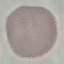

Malaria status: uninfected. Acquired by smartphone through the microscope eyepiece. Cell patch, automatically extracted from a larger field of view and resized to 64 × 64 pixels. Giemsa-stained preparation. Thin blood smear.